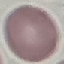

malaria status = uninfected
image type = cell patch, automatically extracted from a larger field of view and resized to 64 × 64 pixels
capture = smartphone camera at the microscope eyepiece
stain = Giemsa
preparation = thin blood film